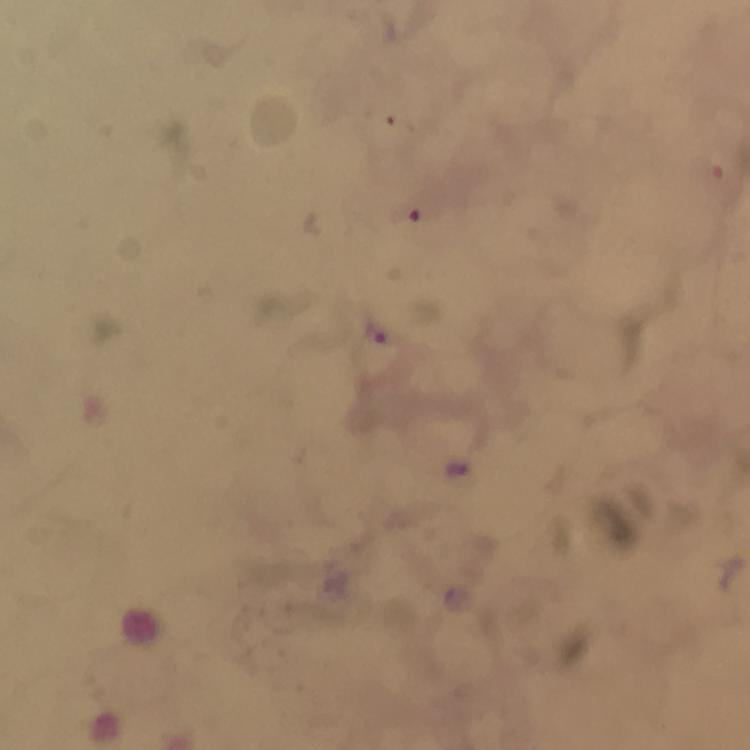
Approximate centers as {x, y} in pixels.
Summary:
  - Plasmodium parasite locations: {374, 332}
  - Image size: 750×750 pixels
  - Magnification: 100x
  - Context: from a malaria diagnostic workup
  - Stain: Giemsa
  - Immersion oil: applied
  - Cropped from: one field of view
  - Preparation: thick blood film
  - Capture: smartphone photograph through a microscope